Locate every malaria parasite.
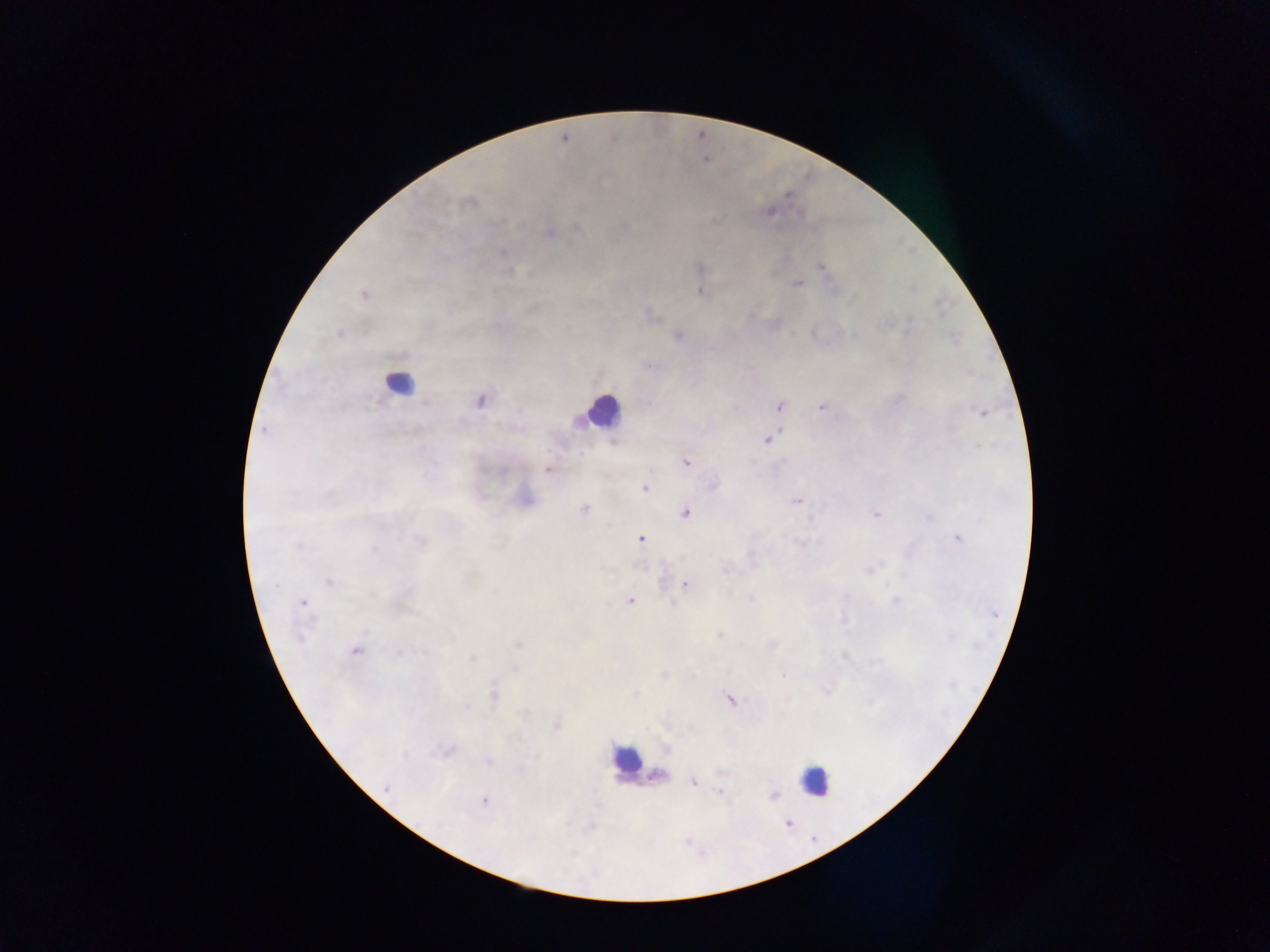
Approximate centers as (x, y) in pixels.
Malaria parasites: (706, 160), (787, 196), (468, 202), (769, 211), (713, 221), (548, 233), (503, 253), (820, 267), (699, 268), (508, 271), (797, 284), (700, 292), (364, 295), (910, 319), (883, 325), (338, 334), (677, 336), (649, 365), (899, 398), (479, 400), (649, 404), (779, 406), (821, 407), (981, 413), (263, 430), (767, 439), (978, 446), (580, 453), (783, 461), (686, 462), (547, 469), (713, 485), (644, 488), (796, 501), (584, 510), (685, 512), (875, 514), (929, 517), (957, 538), (640, 539), (421, 541), (797, 542), (298, 547), (373, 549), (752, 558), (725, 570), (869, 570), (328, 582), (686, 585), (750, 598), (630, 601), (895, 601), (303, 603), (995, 615), (844, 620), (718, 635), (299, 637), (951, 637), (517, 644), (772, 645), (355, 651), (398, 653), (423, 653), (472, 658), (514, 669), (782, 674), (663, 675), (826, 691), (494, 696), (731, 700), (871, 702), (467, 706), (557, 725), (692, 729), (666, 749), (445, 751), (405, 755), (488, 762), (721, 771), (692, 782), (387, 787), (720, 793), (774, 796), (484, 801), (788, 823).

Leukocyte locations: (396, 382), (604, 410), (625, 758), (658, 776), (814, 779). Image is 1270×952 pixels. One field of view. Mobile-phone photograph taken through the microscope. Sample from Ghana. Thick blood smear.